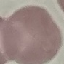
Summary:
  - Malaria status: uninfected
  - Stain: Giemsa
  - Capture: smartphone camera at the microscope eyepiece
  - Image type: automatically extracted cell patch, resized to 64 × 64 pixels
  - Preparation: thin smear